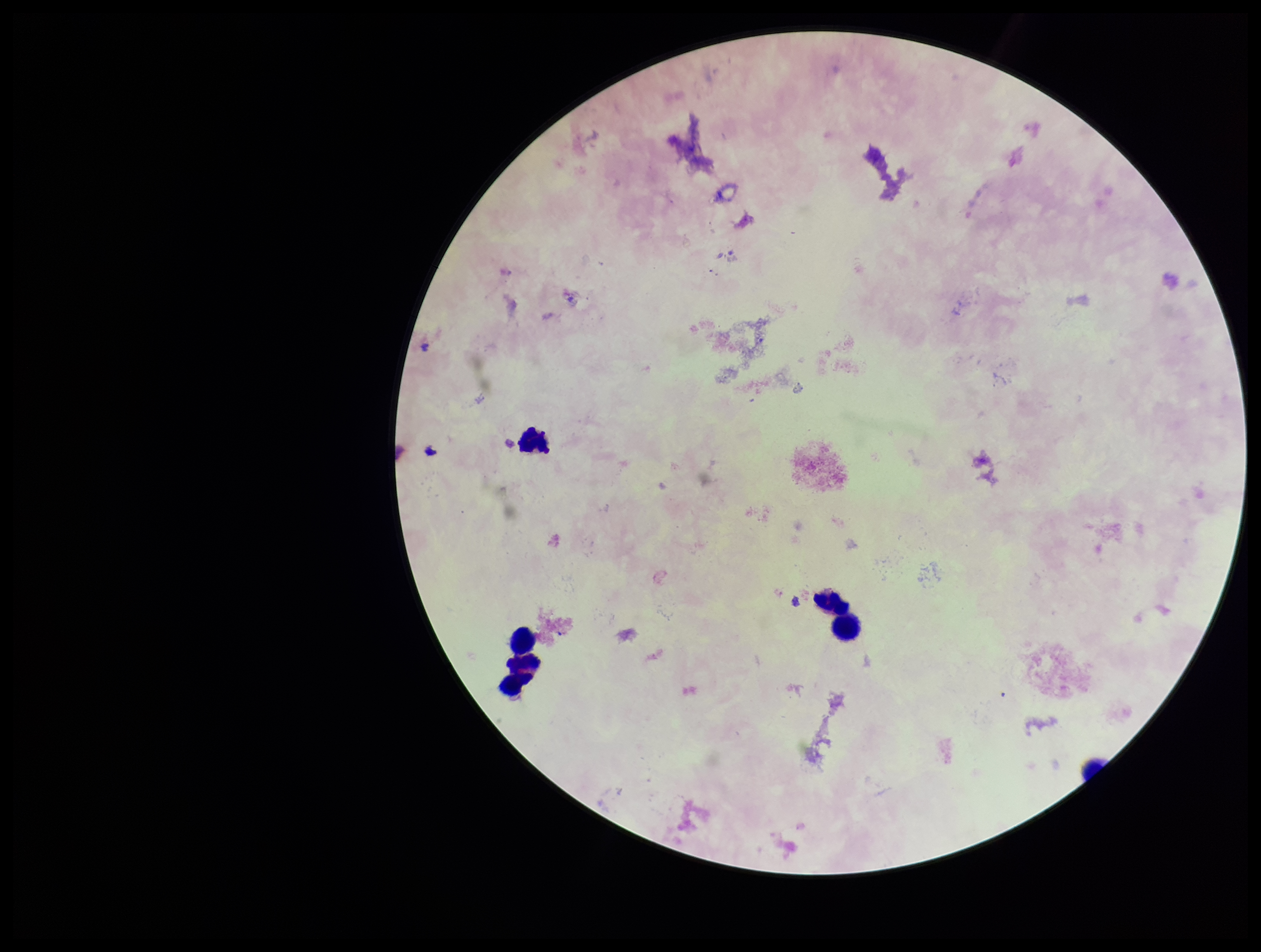

image size = 1261×952 pixels
Plasmodium parasites = none seen
preparation = thick blood smear
parasite count = 0
field of view = single
stain = Giemsa
leukocyte count = 6
capture = smartphone photograph through the microscope eyepiece
patient malaria status = infected
species reported for this patient = Plasmodium falciparum